Assess this cell for malaria.
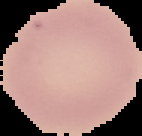
It is uninfected.

Image is 142×136 pixels. Segmented cell region on a black background. From a thin blood film.